Classify this cell by malaria status.
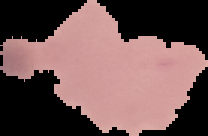

It is uninfected.

{
  "image_size": "208×136 pixels",
  "preparation": "thin blood film",
  "image_type": "segmented cell region with the area outside set to black"
}